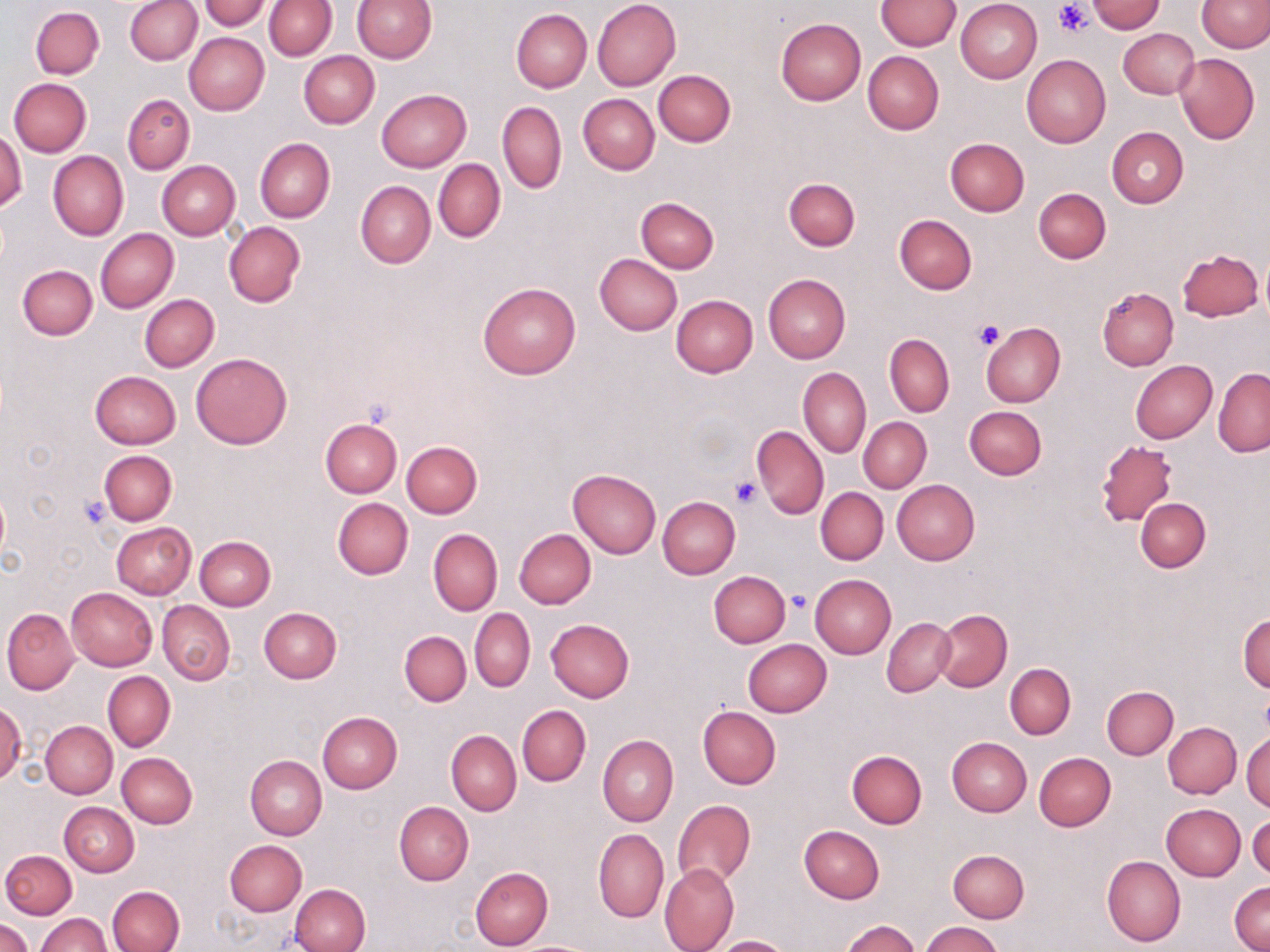
slide-level diagnosis = negative for blood parasites
field of view = single
modality = light microscopy
image size = 1270×952 pixels
platelet locations = approximate bounding boxes as [x1, y1, x2, y2] in pixels: [1055, 2, 1093, 37], [973, 320, 1004, 352], [730, 476, 763, 507], [78, 495, 111, 527], [785, 590, 813, 613]
uninfected red blood cell locations = approximate bounding boxes as [x1, y1, x2, y2] in pixels: [201, 0, 269, 30], [352, 0, 435, 62], [1196, 0, 1269, 53], [125, 1, 202, 65], [264, 1, 336, 59], [592, 1, 680, 89], [875, 1, 960, 51], [955, 1, 1042, 83], [1086, 1, 1167, 34], [31, 6, 105, 79], [511, 8, 592, 92], [775, 18, 867, 104], [1119, 27, 1199, 98], [184, 33, 269, 115], [298, 51, 379, 128], [862, 51, 944, 134], [1021, 53, 1111, 148], [1174, 53, 1259, 145], [653, 69, 735, 147], [9, 78, 91, 156], [377, 89, 471, 172], [124, 94, 195, 174], [579, 94, 659, 175], [498, 101, 567, 194], [1107, 127, 1188, 208], [0, 129, 27, 212], [255, 137, 335, 222], [945, 138, 1029, 216], [48, 150, 128, 241], [434, 159, 505, 242], [156, 160, 241, 240], [782, 178, 860, 251], [356, 180, 435, 268], [1033, 188, 1111, 264], [636, 196, 719, 273], [894, 214, 978, 293], [224, 222, 305, 307], [95, 228, 178, 313], [1178, 248, 1265, 322], [595, 253, 682, 335], [17, 265, 97, 340], [763, 273, 851, 363], [478, 281, 581, 379], [1097, 287, 1178, 370], [140, 294, 219, 371], [670, 295, 759, 377], [980, 323, 1065, 407], [884, 334, 954, 417], [875, 335, 946, 494], [191, 353, 292, 449], [1130, 361, 1217, 443], [799, 367, 870, 458], [1214, 368, 1270, 456], [90, 370, 181, 448], [964, 406, 1046, 479], [858, 417, 931, 493], [321, 418, 402, 497], [751, 425, 829, 518], [401, 441, 482, 518], [1096, 442, 1181, 526], [100, 450, 177, 525], [568, 468, 661, 559], [891, 479, 980, 564], [816, 488, 888, 564], [657, 496, 740, 579], [332, 497, 413, 580], [1136, 498, 1210, 572], [111, 523, 196, 599], [514, 528, 596, 608], [428, 529, 502, 615], [195, 535, 275, 609], [709, 570, 791, 647], [810, 574, 896, 658], [67, 587, 158, 671], [157, 600, 235, 684], [2, 608, 80, 696], [259, 608, 341, 683], [470, 608, 535, 692], [933, 609, 1011, 691], [1238, 612, 1269, 693], [882, 618, 955, 696], [545, 620, 635, 702], [399, 631, 471, 707], [743, 639, 831, 717], [1005, 663, 1076, 739], [102, 671, 175, 751], [68, 682, 170, 772], [1101, 686, 1179, 760], [0, 700, 24, 785], [517, 704, 591, 787], [698, 707, 780, 789], [317, 712, 402, 793], [41, 720, 117, 798], [1163, 722, 1241, 798], [446, 729, 521, 815], [1242, 730, 1270, 812], [598, 735, 678, 826], [947, 736, 1031, 816], [846, 750, 926, 828], [117, 752, 197, 828], [1034, 752, 1115, 830], [245, 755, 327, 840], [673, 799, 756, 889], [60, 802, 138, 876], [393, 802, 472, 885], [1162, 804, 1245, 881], [1248, 814, 1270, 878], [800, 825, 885, 904], [593, 829, 668, 924], [224, 840, 306, 915], [2, 849, 76, 919], [948, 849, 1029, 922], [1102, 855, 1186, 946], [660, 863, 739, 952], [470, 867, 553, 950], [1229, 881, 1269, 951], [289, 883, 370, 952], [107, 885, 185, 952], [35, 913, 111, 952], [0, 918, 33, 952], [840, 920, 921, 952], [920, 921, 1004, 952], [712, 935, 795, 952], [511, 940, 600, 952]
stain = May-Grünwald-Giemsa
preparation = thin blood smear
magnification = 1000x